State which parasite is depicted.
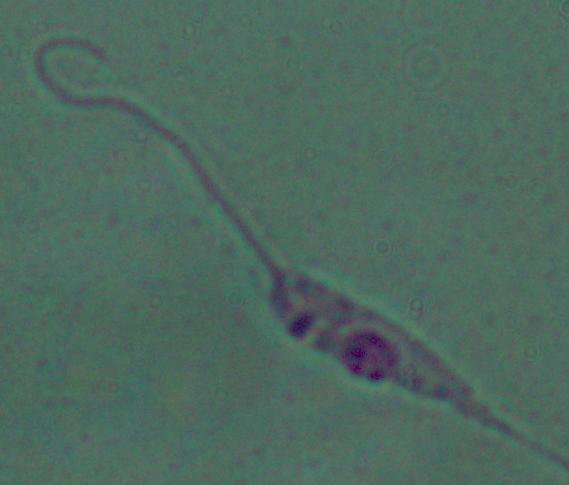
This is Leishmania.

modality = micrograph
magnification = 1000x